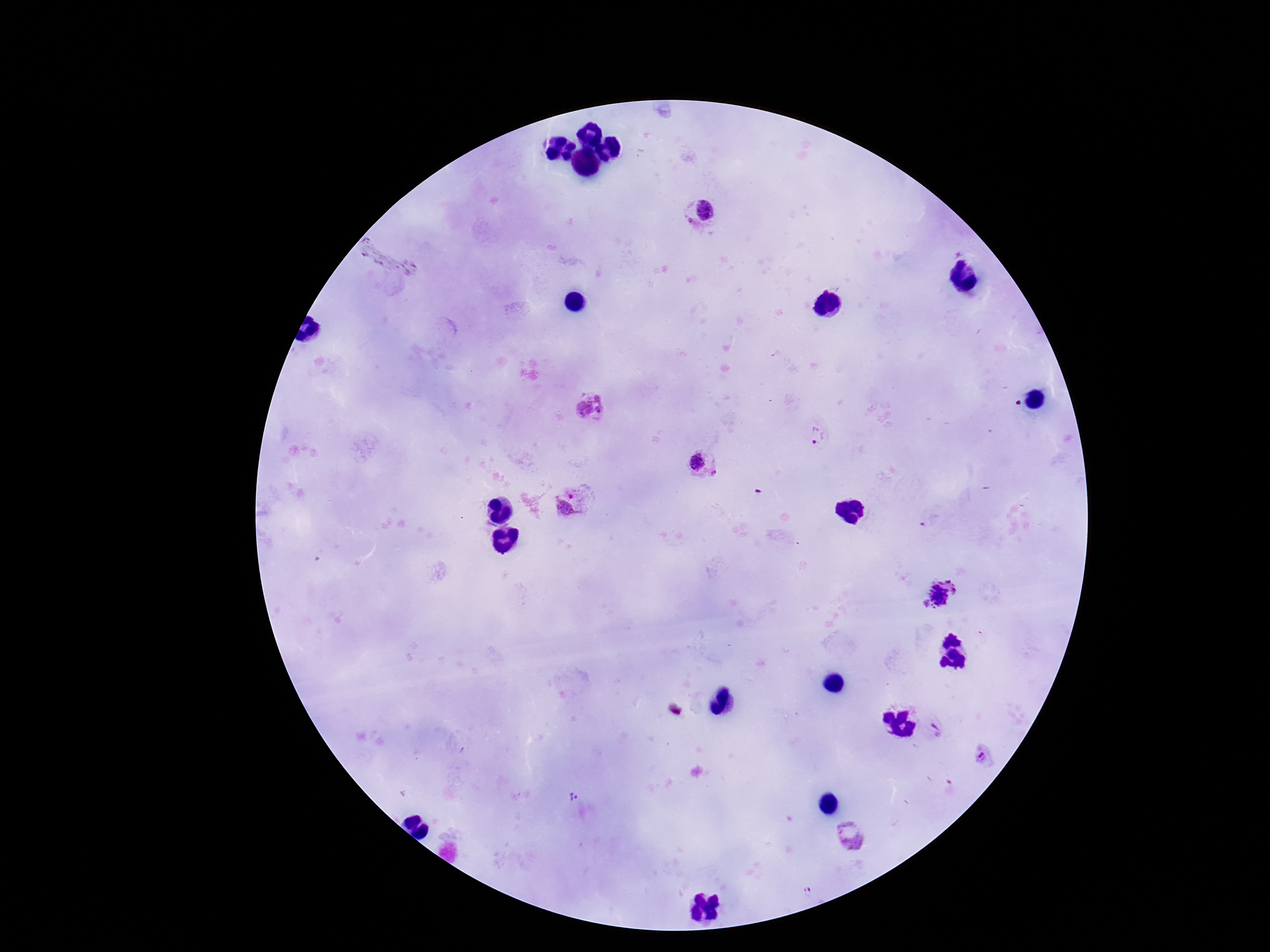
Approximate centers as (x, y) in pixels.
Summary:
  - Plasmodium parasite locations: (700, 215), (590, 404), (817, 435), (704, 465), (573, 502), (941, 593), (937, 728), (984, 759), (574, 797), (850, 833), (809, 892)
  - Magnification: 100x
  - Capture: smartphone camera through the microscope eyepiece
  - Patient malaria status: infected
  - Preparation: thick blood smear
  - Stain: Giemsa
  - Field of view: one from this slide
  - Image size: 1270×952 pixels